Locate every Plasmodium parasite and identify its life-cycle stage.
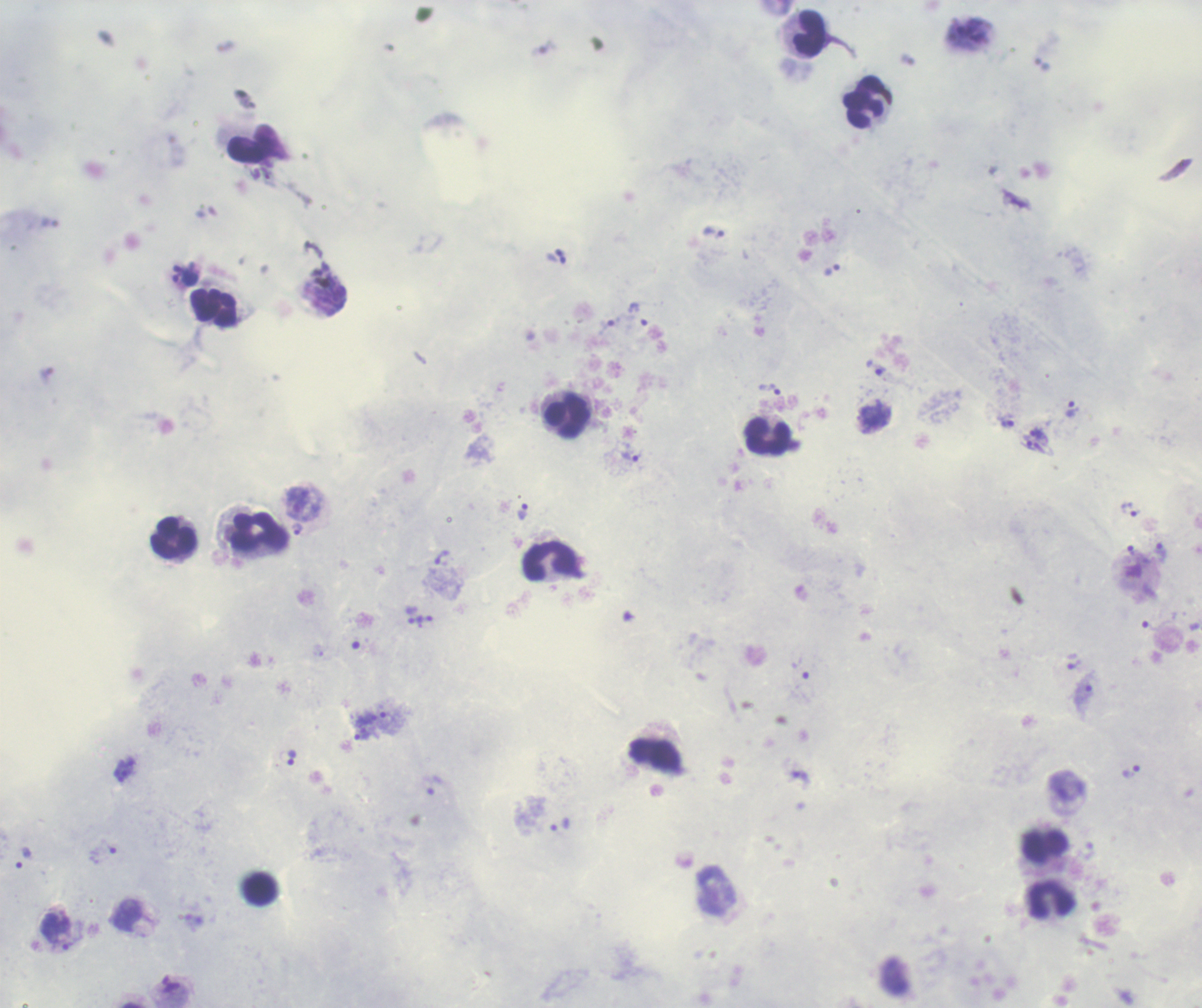

Approximate centers as [x, y] in pixels.
Trophozoites: [831, 270], [186, 278], [638, 314], [875, 367], [769, 389], [1071, 409], [1007, 422], [1038, 433], [1035, 445], [632, 456], [296, 502], [1131, 510], [522, 512], [297, 529], [1132, 551], [1159, 553], [442, 558], [427, 617], [1074, 665], [1083, 696], [372, 718], [362, 736], [292, 757], [1131, 772], [434, 786], [560, 824], [23, 859], [55, 931].
No schizont or gametocyte forms observed.

Approximate centers as [x, y] in pixels. Leukocyte locations: [809, 34], [863, 102], [252, 143], [214, 307], [568, 416], [768, 436], [259, 532], [173, 537], [550, 561], [1046, 846], [1052, 900]. Single field of view. Romanowsky-stained preparation. Background quality: unsatisfactory. Previously used in an actual diagnosis. Captured at 100x magnification. Thick blood film. Coloration quality: good. Image is 1202×1008 pixels.